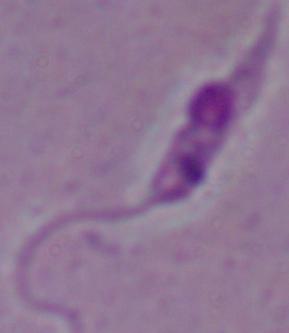
A Leishmania parasite is shown. Captured at 1000x magnification. Photomicrograph.